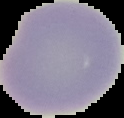

result = no Plasmodium parasites detected
image type = cell region segmented out of the field of view; surrounding area masked to black
preparation = thin blood smear
image size = 124×118 pixels